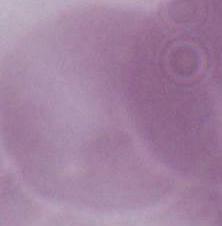

{
  "magnification": "1000x",
  "modality": "photomicrograph",
  "identification": "erythrocyte"
}